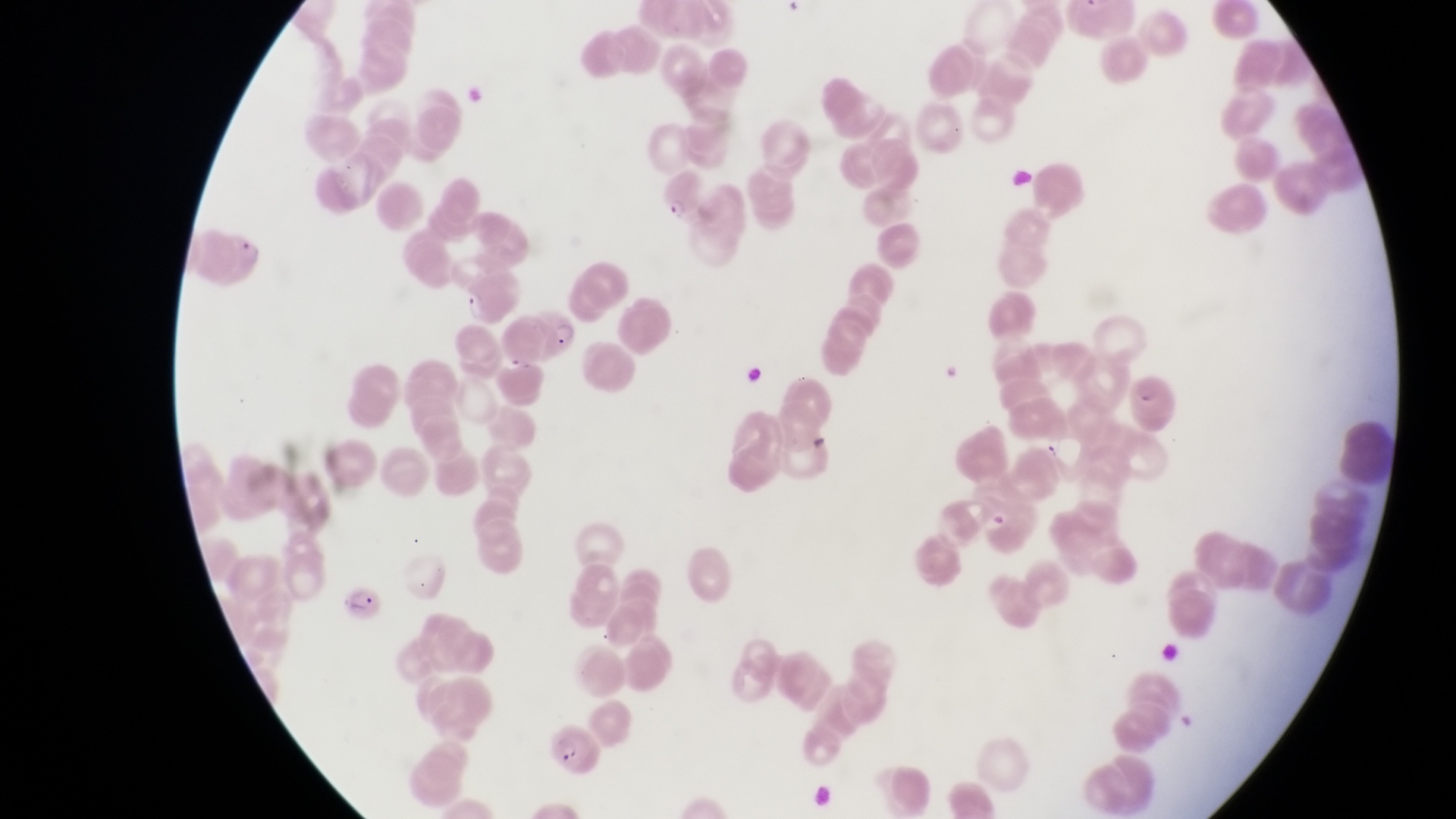
Approximate bounding boxes as {left, top, right, bottom} in pixels. Artifact (platelet-like body, stain precipitate, or debris) locations: {1003, 165, 1037, 192}, {935, 360, 964, 384}, {742, 362, 772, 385}, {984, 505, 1014, 535}. Parasitised red blood cell locations: {658, 166, 708, 222}, {218, 228, 273, 288}, {535, 297, 584, 358}, {1128, 367, 1183, 433}, {343, 581, 398, 627}, {547, 726, 607, 776}. Sample from Uganda. Image is 1456×819 pixels. Single field of view. Thin blood film. At a magnification of 1000x. Photographed through the eyepiece of an Olympus CX-23 microscope with a smartphone camera.